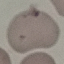
Result: no malaria parasites detected. Automatically extracted cell patch, resized to 64 × 64 pixels. Thin smear of blood. Photographed with a smartphone camera at the microscope eyepiece. Giemsa-stained preparation.